Locate and identify every blood parasite.
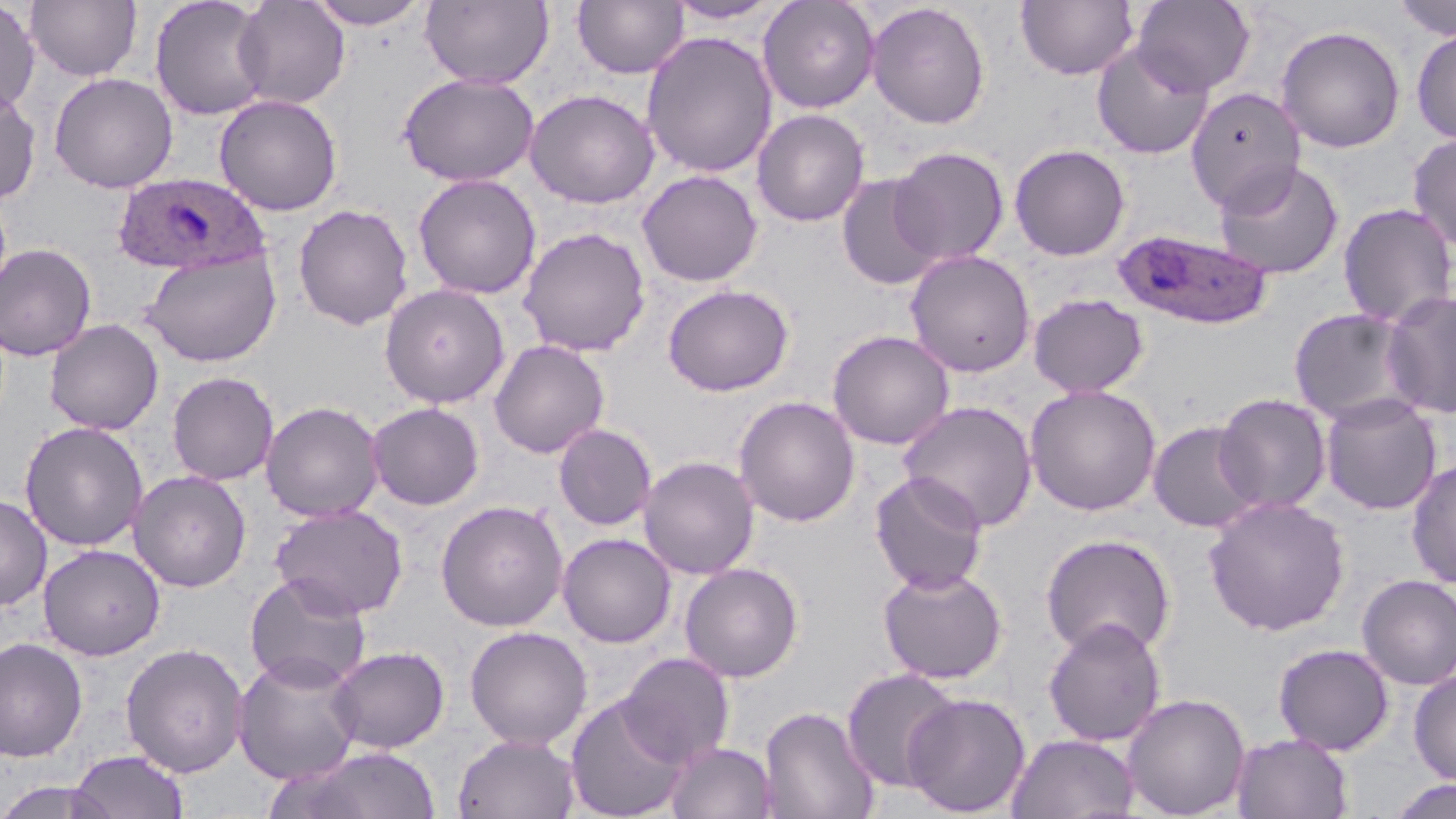
Approximate bounding boxes as [x1, y1, x2, y2] in pixels.
Plasmodium ovale-infected red blood cells: [112, 171, 270, 276], [1111, 228, 1275, 330].
No Plasmodium falciparum, Plasmodium malariae, Plasmodium vivax, Babesia divergens, or Trypanosoma brucei observed.

Uninfected red blood cell locations: [25, 0, 142, 82], [149, 0, 272, 121], [232, 0, 350, 109], [305, 0, 430, 29], [420, 0, 554, 89], [571, 0, 689, 79], [663, 0, 788, 25], [758, 0, 881, 113], [1132, 0, 1256, 95], [1392, 0, 1456, 40], [0, 1, 40, 116], [1015, 1, 1139, 80], [866, 2, 990, 130], [1275, 25, 1406, 153], [1411, 28, 1456, 145], [641, 31, 778, 179], [1092, 41, 1214, 159], [48, 72, 178, 193], [400, 73, 539, 187], [0, 85, 41, 206], [1186, 86, 1305, 214], [525, 89, 659, 209], [213, 94, 342, 216], [752, 109, 870, 227], [1407, 133, 1456, 251], [1009, 144, 1130, 261], [889, 146, 1009, 265], [1213, 160, 1344, 280], [636, 170, 764, 287], [412, 173, 541, 300], [836, 173, 945, 291], [1338, 203, 1456, 329], [293, 204, 414, 330], [518, 227, 651, 357], [0, 242, 97, 361], [141, 249, 281, 367], [905, 250, 1036, 378], [380, 284, 509, 409], [662, 284, 794, 396], [1382, 290, 1456, 418], [1028, 294, 1148, 398], [1288, 308, 1421, 426], [44, 319, 164, 434], [827, 330, 955, 449], [488, 340, 610, 458], [167, 371, 279, 485], [1024, 384, 1162, 516], [1213, 393, 1332, 514], [1320, 393, 1442, 515], [733, 396, 861, 527], [898, 400, 1038, 532], [261, 401, 384, 522], [366, 402, 484, 510], [1147, 420, 1262, 533], [19, 421, 149, 551], [553, 423, 657, 530], [638, 455, 759, 580], [1406, 458, 1456, 589], [129, 470, 251, 592], [870, 471, 988, 595], [0, 494, 52, 611], [1203, 496, 1351, 636], [435, 500, 568, 632], [270, 503, 409, 619], [558, 533, 675, 647], [1040, 533, 1176, 659], [38, 544, 165, 660], [679, 562, 804, 682], [877, 565, 1008, 684], [244, 572, 372, 692], [1356, 574, 1456, 690], [1042, 617, 1167, 747], [464, 625, 592, 749], [0, 637, 88, 763], [120, 642, 249, 778], [1273, 643, 1394, 755], [327, 645, 450, 753], [233, 652, 365, 785], [618, 652, 735, 766], [841, 668, 961, 793], [1409, 669, 1456, 786], [1121, 692, 1250, 819], [902, 693, 1031, 817], [565, 694, 691, 819], [759, 704, 880, 819], [453, 733, 582, 818], [1006, 733, 1140, 819], [1231, 733, 1354, 819], [665, 742, 777, 819], [297, 747, 442, 819], [68, 750, 189, 819], [1384, 777, 1456, 819], [0, 778, 123, 819]. Slide-level diagnosis: Plasmodium ovale. Image is 1456×819 pixels. Captured at 1000x magnification. Thin blood film. Single field of view. Light microscopy. May-Grünwald-Giemsa-stained preparation.